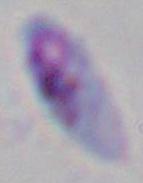

Micrograph. 1000x magnification. Toxoplasma gondii is seen.